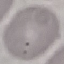

malaria status = uninfected
preparation = thin blood smear
image type = cell patch, automatically extracted from a larger field of view and resized to 64 × 64 pixels
stain = Giemsa
capture = smartphone camera at the microscope eyepiece